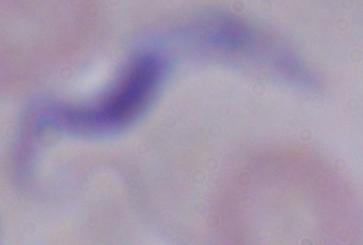

identification = trypanosome
modality = photomicrograph
magnification = 1000x